Outline each Plasmodium falciparum-infected red blood cell.
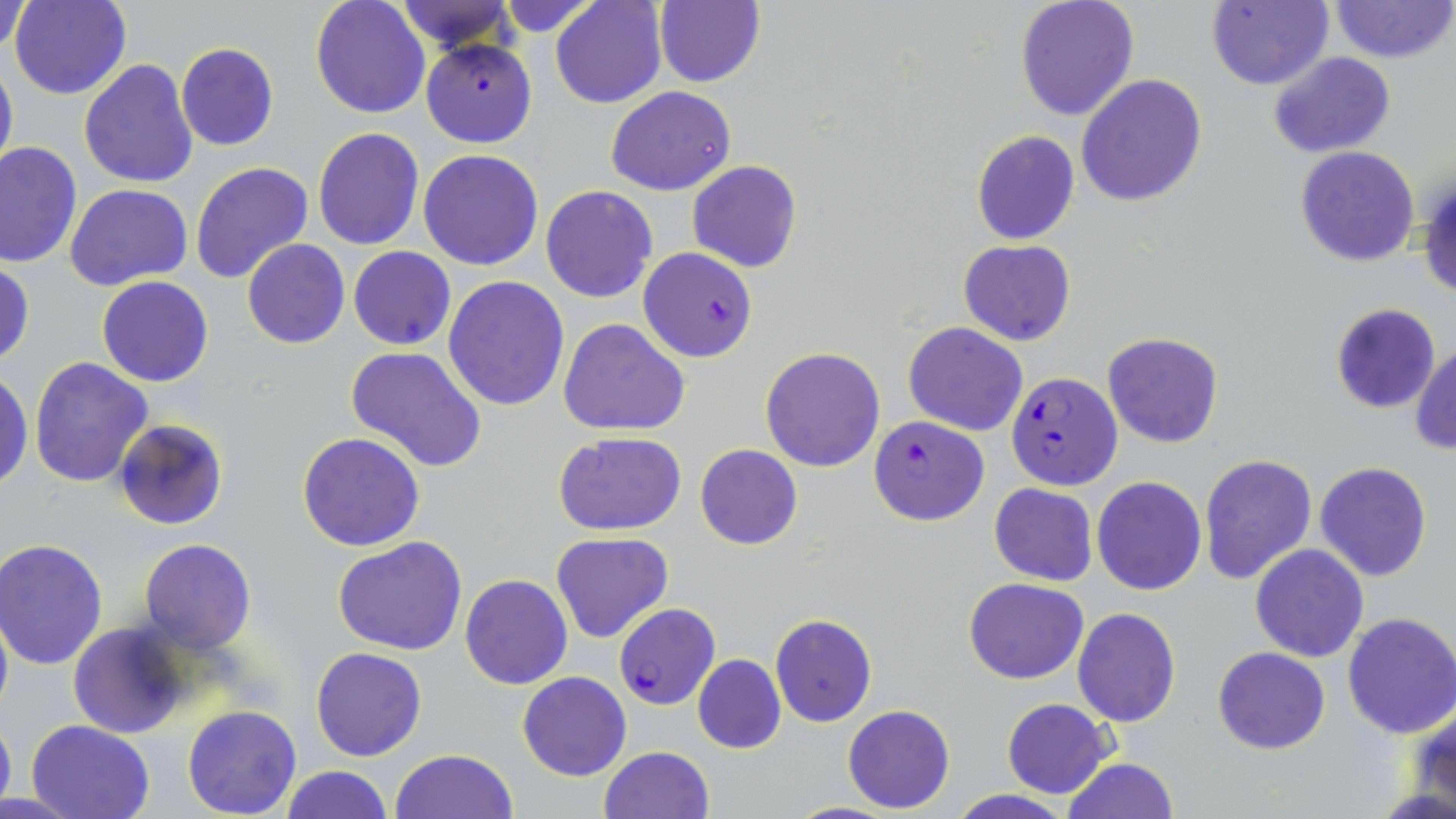

Approximate bounding boxes as named x1/y1/x2/y2 corners in pixels.
Plasmodium falciparum-infected red blood cells: (x1=421, y1=38, x2=538, y2=148), (x1=638, y1=247, x2=758, y2=362), (x1=1005, y1=371, x2=1122, y2=489), (x1=869, y1=415, x2=988, y2=526), (x1=614, y1=603, x2=719, y2=709).

slide-level diagnosis = Plasmodium falciparum
modality = optical microscopy
stain = May-Grünwald-Giemsa
field of view = single
uninfected red blood cell locations = approximate bounding boxes as named x1/y1/x2/y2 corners in pixels: (x1=9, y1=0, x2=131, y2=100), (x1=310, y1=0, x2=432, y2=120), (x1=391, y1=0, x2=519, y2=54), (x1=551, y1=0, x2=667, y2=109), (x1=1014, y1=0, x2=1140, y2=122), (x1=1206, y1=0, x2=1333, y2=91), (x1=1329, y1=0, x2=1455, y2=64), (x1=493, y1=1, x2=602, y2=35), (x1=652, y1=1, x2=766, y2=87), (x1=2, y1=3, x2=34, y2=55), (x1=175, y1=43, x2=279, y2=151), (x1=1268, y1=51, x2=1395, y2=158), (x1=0, y1=54, x2=17, y2=180), (x1=79, y1=59, x2=198, y2=189), (x1=1077, y1=75, x2=1207, y2=208), (x1=606, y1=87, x2=735, y2=196), (x1=311, y1=127, x2=425, y2=251), (x1=971, y1=130, x2=1079, y2=244), (x1=1, y1=142, x2=82, y2=269), (x1=1295, y1=146, x2=1420, y2=266), (x1=418, y1=149, x2=544, y2=271), (x1=687, y1=160, x2=802, y2=273), (x1=189, y1=161, x2=313, y2=285), (x1=1419, y1=171, x2=1456, y2=303), (x1=66, y1=183, x2=193, y2=292), (x1=541, y1=184, x2=658, y2=303), (x1=242, y1=239, x2=349, y2=349), (x1=957, y1=240, x2=1076, y2=346), (x1=348, y1=246, x2=456, y2=350), (x1=0, y1=260, x2=35, y2=368), (x1=96, y1=276, x2=214, y2=387), (x1=442, y1=276, x2=569, y2=411), (x1=1329, y1=303, x2=1441, y2=413), (x1=558, y1=318, x2=691, y2=436), (x1=903, y1=322, x2=1027, y2=436), (x1=1102, y1=332, x2=1223, y2=448), (x1=1411, y1=344, x2=1455, y2=455), (x1=345, y1=346, x2=487, y2=472), (x1=760, y1=347, x2=885, y2=472), (x1=29, y1=356, x2=155, y2=487), (x1=0, y1=373, x2=33, y2=490), (x1=114, y1=419, x2=228, y2=530), (x1=554, y1=430, x2=687, y2=536), (x1=296, y1=432, x2=425, y2=551), (x1=695, y1=444, x2=803, y2=549), (x1=1198, y1=453, x2=1317, y2=584), (x1=1315, y1=461, x2=1433, y2=583), (x1=1091, y1=476, x2=1207, y2=596), (x1=988, y1=483, x2=1098, y2=585), (x1=551, y1=531, x2=672, y2=643), (x1=332, y1=536, x2=470, y2=656), (x1=138, y1=537, x2=257, y2=654), (x1=2, y1=538, x2=111, y2=670), (x1=1249, y1=544, x2=1369, y2=662), (x1=460, y1=574, x2=572, y2=690), (x1=963, y1=578, x2=1088, y2=684), (x1=0, y1=602, x2=12, y2=723), (x1=1072, y1=607, x2=1180, y2=726), (x1=1340, y1=611, x2=1456, y2=739), (x1=770, y1=613, x2=876, y2=726), (x1=69, y1=621, x2=189, y2=739), (x1=1212, y1=646, x2=1330, y2=753), (x1=311, y1=648, x2=426, y2=762), (x1=693, y1=654, x2=786, y2=754), (x1=517, y1=671, x2=632, y2=782), (x1=1002, y1=698, x2=1114, y2=799), (x1=1410, y1=700, x2=1456, y2=816), (x1=181, y1=703, x2=302, y2=818), (x1=842, y1=704, x2=955, y2=813), (x1=0, y1=707, x2=15, y2=816), (x1=28, y1=719, x2=154, y2=819), (x1=598, y1=746, x2=713, y2=819), (x1=391, y1=749, x2=517, y2=819), (x1=1062, y1=758, x2=1181, y2=818), (x1=279, y1=765, x2=392, y2=819), (x1=950, y1=789, x2=1072, y2=819)
image size = 1456×819 pixels
preparation = thin blood smear
magnification = 1000x